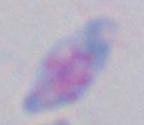 Micrograph. Captured at 1000x magnification. Toxoplasma gondii is shown.